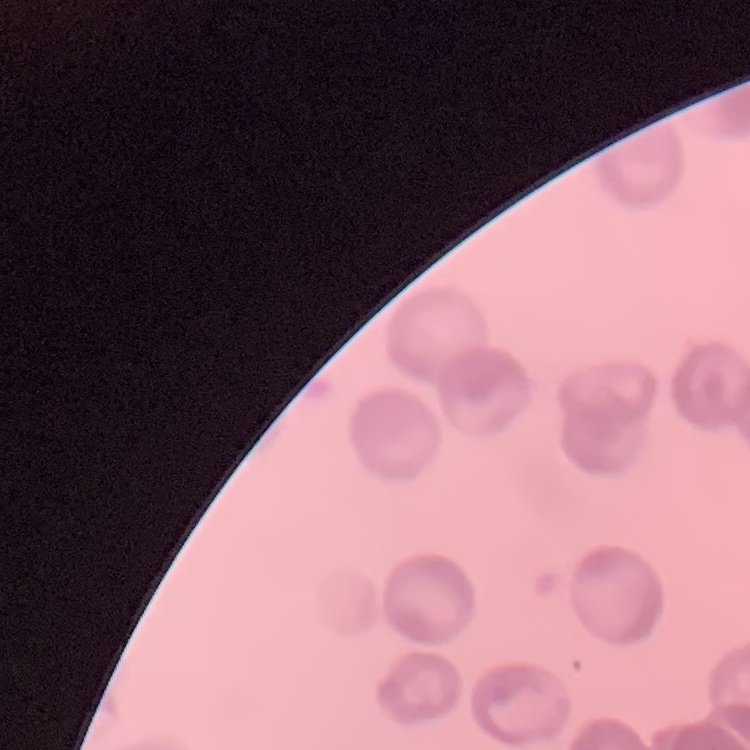
Summary:
  - Red blood cell morphology: rouleaux formation
  - Image type: one tile cut from a larger photomicrograph
  - Preparation: thin blood film
  - Stain: Field's or Giemsa